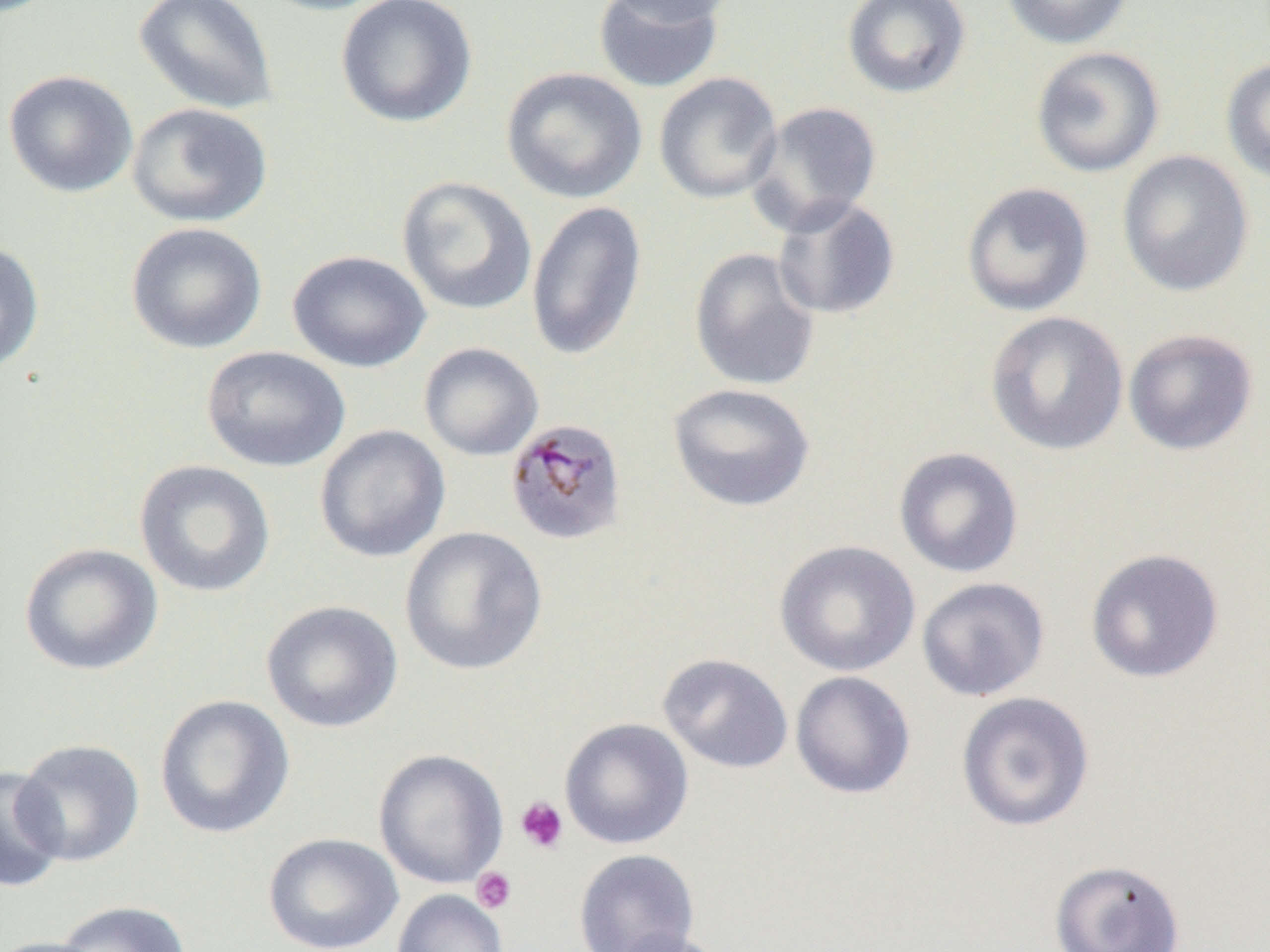 Approximate bounding boxes as (x1,y1)-(x2,y2) corner pairs in pixels. Plasmodium malariae-infected red blood cell locations: (504,417)-(627,547). Platelet locations: (515,796)-(569,854), (471,867)-(517,913). Uninfected red blood cell locations: (132,0)-(279,115), (252,0)-(394,16), (336,0)-(478,128), (597,0)-(740,26), (841,0)-(972,100), (1000,0)-(1135,49), (592,1)-(725,93), (1030,45)-(1165,178), (1221,56)-(1270,186), (501,67)-(647,204), (2,69)-(138,198), (653,72)-(783,204), (747,101)-(883,235), (127,102)-(273,227), (1116,150)-(1255,298), (396,175)-(537,316), (961,181)-(1095,317), (771,196)-(901,320), (525,199)-(647,362), (126,222)-(267,354), (0,241)-(45,375), (689,247)-(821,392), (287,249)-(431,373), (984,310)-(1129,456), (1123,328)-(1260,456), (418,342)-(544,461), (201,346)-(350,472), (667,382)-(815,512), (314,424)-(451,563), (893,446)-(1024,578), (134,459)-(276,598), (399,526)-(547,675), (774,539)-(920,677), (19,542)-(163,676), (1085,548)-(1225,684), (916,577)-(1050,701), (261,600)-(403,733), (657,653)-(793,774), (790,670)-(916,799), (955,692)-(1096,832), (155,694)-(295,839), (559,717)-(694,850), (13,738)-(145,867), (373,749)-(508,889), (0,766)-(67,893), (263,832)-(404,952), (573,848)-(700,952), (1049,859)-(1186,952), (391,889)-(508,952), (52,900)-(192,951), (607,929)-(735,952), (0,937)-(109,952). Slide-level diagnosis: Plasmodium malariae. Captured at 1000x magnification. Light microscopy. One field of a larger specimen. Thin blood smear. Image is 1270×952 pixels.